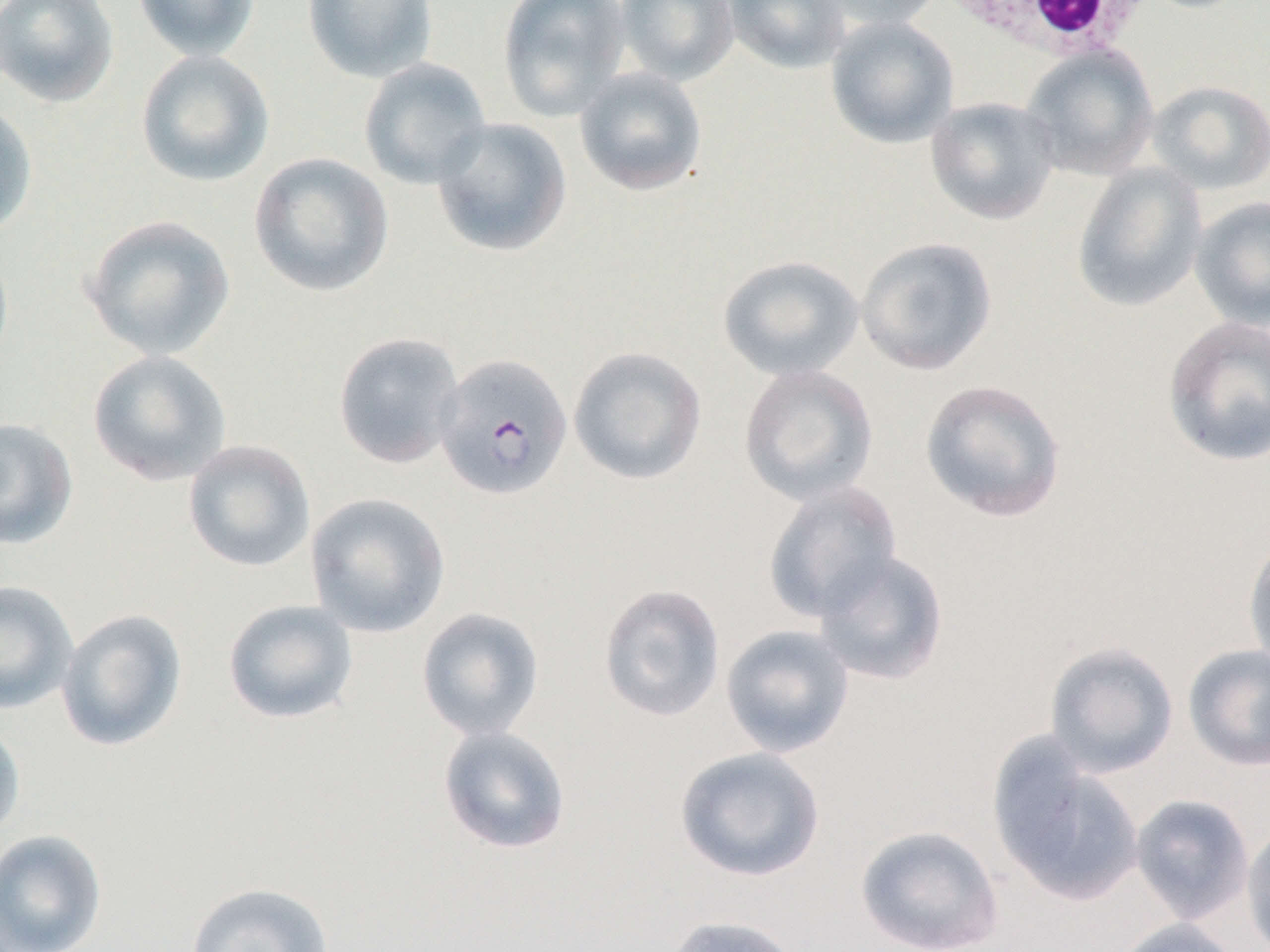

Summary:
  - Coordinate format: approximate bounding boxes as named x1/y1/x2/y2 corners in pixels
  - Plasmodium falciparum-infected red blood cell locations: (x1=433, y1=352, x2=573, y2=500)
  - White blood cell locations: (x1=933, y1=0, x2=1160, y2=63)
  - Uninfected red blood cell locations: (x1=0, y1=0, x2=119, y2=107), (x1=132, y1=0, x2=260, y2=62), (x1=302, y1=0, x2=438, y2=83), (x1=497, y1=0, x2=631, y2=122), (x1=614, y1=0, x2=740, y2=85), (x1=723, y1=0, x2=851, y2=73), (x1=809, y1=0, x2=945, y2=32), (x1=825, y1=16, x2=959, y2=149), (x1=1020, y1=45, x2=1159, y2=181), (x1=135, y1=49, x2=275, y2=188), (x1=358, y1=57, x2=492, y2=190), (x1=574, y1=66, x2=708, y2=196), (x1=1147, y1=80, x2=1270, y2=195), (x1=925, y1=96, x2=1061, y2=225), (x1=0, y1=100, x2=38, y2=239), (x1=431, y1=117, x2=572, y2=258), (x1=249, y1=152, x2=394, y2=297), (x1=1071, y1=163, x2=1207, y2=313), (x1=1190, y1=196, x2=1270, y2=331), (x1=80, y1=214, x2=236, y2=361), (x1=855, y1=236, x2=997, y2=376), (x1=717, y1=255, x2=864, y2=382), (x1=1162, y1=315, x2=1270, y2=468), (x1=332, y1=331, x2=466, y2=470), (x1=569, y1=346, x2=707, y2=486), (x1=87, y1=350, x2=232, y2=486), (x1=738, y1=363, x2=879, y2=506), (x1=919, y1=378, x2=1067, y2=523), (x1=0, y1=417, x2=79, y2=551), (x1=182, y1=439, x2=316, y2=573), (x1=761, y1=480, x2=903, y2=624), (x1=304, y1=492, x2=451, y2=638), (x1=1242, y1=531, x2=1270, y2=676), (x1=812, y1=549, x2=950, y2=685), (x1=0, y1=580, x2=78, y2=714), (x1=597, y1=582, x2=726, y2=722), (x1=222, y1=599, x2=359, y2=724), (x1=416, y1=607, x2=545, y2=741), (x1=56, y1=608, x2=188, y2=752), (x1=720, y1=624, x2=855, y2=758), (x1=1043, y1=640, x2=1179, y2=778), (x1=1182, y1=644, x2=1270, y2=772), (x1=0, y1=718, x2=26, y2=843), (x1=437, y1=725, x2=572, y2=855), (x1=987, y1=740, x2=1144, y2=906), (x1=675, y1=746, x2=826, y2=882), (x1=1130, y1=794, x2=1254, y2=925), (x1=1242, y1=822, x2=1270, y2=952), (x1=854, y1=824, x2=1005, y2=952), (x1=0, y1=829, x2=107, y2=952), (x1=185, y1=882, x2=334, y2=952), (x1=660, y1=914, x2=806, y2=952), (x1=1110, y1=918, x2=1245, y2=952)
  - Slide-level diagnosis: Plasmodium falciparum
  - Modality: light microscopy
  - Image size: 1270×952 pixels
  - Magnification: 1000x
  - Preparation: thin blood smear
  - Field of view: single